Report the malaria status of this cell.
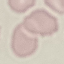
Uninfected.

preparation = thin smear
image type = cell patch, automatically extracted from a larger field of view and resized to 64 × 64 pixels
capture = smartphone through the microscope eyepiece
stain = Giemsa